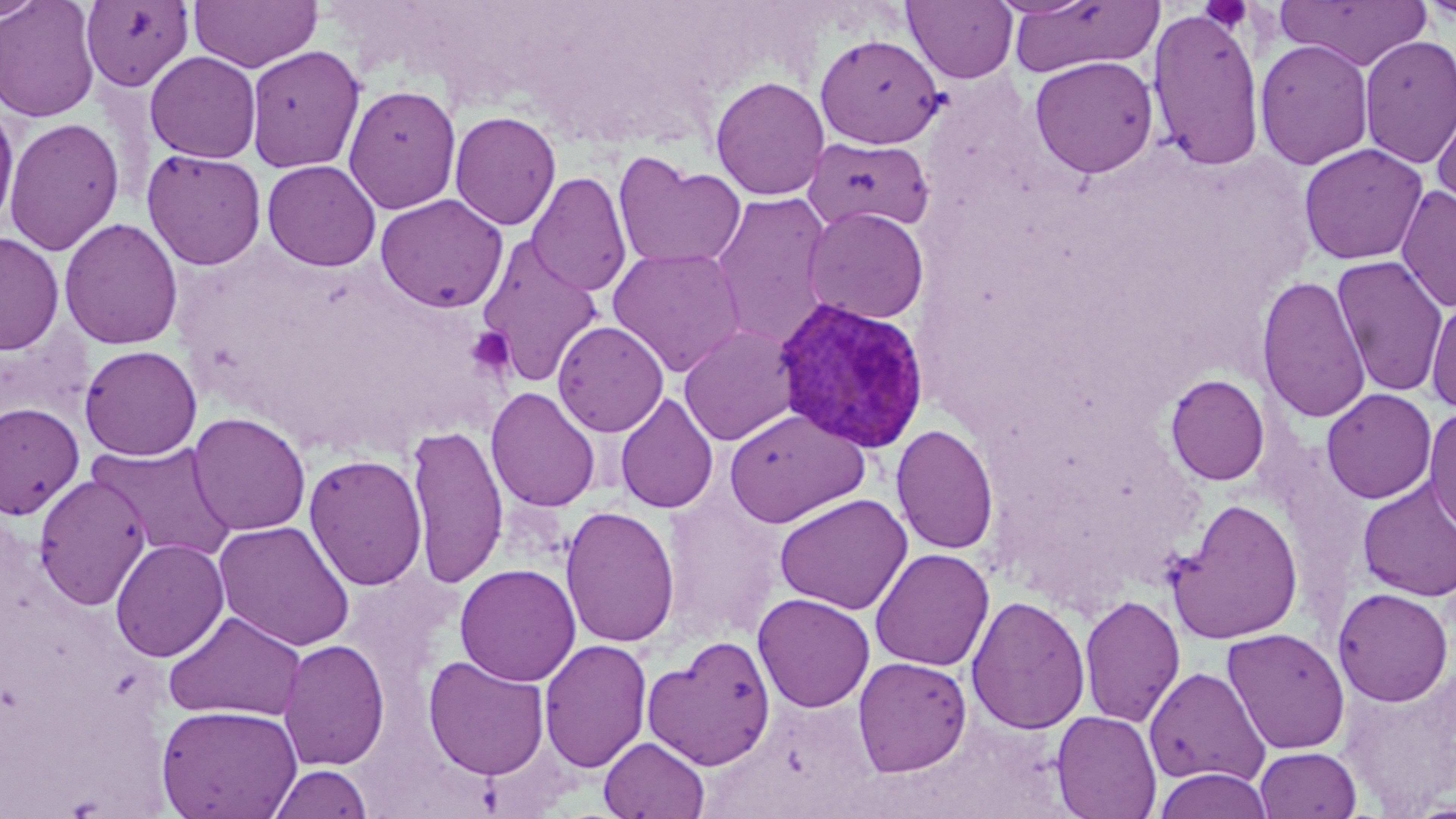
slide_level_diagnosis: Plasmodium vivax
platelet_locations: 'approximate bounding boxes as (x1, y1, x2, y2) in pixels: (1197, 1, 1254, 33), (467, 327, 515, 376)'
modality: light microscopy
stain: May-Grünwald-Giemsa
field_of_view: one of a larger specimen
image_size: 1456×819 pixels
plasmodium_vivax_infected_red_blood_cell_locations: 'approximate bounding boxes as (x1, y1, x2, y2) in pixels: (772, 297, 930, 454)'
preparation: thin blood smear
magnification: 1000x
uninfected_red_blood_cell_locations: 'approximate bounding boxes as (x1, y1, x2, y2) in pixels: (0, 0, 48, 24), (0, 0, 100, 123), (80, 0, 195, 91), (189, 0, 322, 72), (903, 0, 1018, 83), (1006, 0, 1162, 77), (1277, 0, 1431, 70), (1416, 0, 1455, 25), (1147, 8, 1265, 171), (814, 33, 946, 149), (1358, 35, 1456, 168), (1255, 38, 1373, 170), (245, 45, 365, 172), (145, 51, 262, 163), (1029, 55, 1158, 179), (710, 75, 830, 201), (343, 84, 462, 215), (1431, 91, 1456, 215), (0, 100, 20, 233), (448, 111, 562, 230), (3, 116, 124, 255), (802, 136, 934, 233), (1299, 142, 1429, 265), (142, 149, 266, 270), (613, 153, 746, 270), (262, 160, 381, 271), (527, 171, 632, 297), (1396, 184, 1456, 313), (711, 191, 834, 349), (374, 194, 509, 313), (803, 206, 929, 324), (59, 217, 184, 350), (0, 231, 65, 356), (476, 235, 604, 388), (608, 247, 746, 377), (1331, 254, 1449, 397), (1256, 273, 1371, 425), (1425, 294, 1456, 415), (552, 320, 669, 436), (679, 324, 800, 446), (80, 345, 202, 461), (1165, 373, 1270, 486), (486, 386, 601, 512), (1321, 388, 1437, 504), (615, 392, 719, 514), (0, 402, 84, 519), (1423, 404, 1456, 536), (724, 408, 869, 527), (188, 412, 311, 536), (891, 423, 999, 555), (407, 424, 509, 589), (89, 441, 237, 563), (304, 454, 428, 591), (33, 474, 151, 610), (1357, 479, 1456, 601), (774, 493, 912, 615), (1166, 498, 1305, 644), (560, 505, 680, 648), (214, 520, 356, 652), (110, 538, 230, 662), (870, 548, 995, 671), (454, 563, 581, 686), (1333, 587, 1454, 706), (753, 593, 875, 712), (1078, 594, 1186, 728), (966, 595, 1090, 735), (164, 610, 307, 722), (1222, 627, 1350, 755), (643, 635, 777, 771), (278, 638, 390, 770), (539, 638, 652, 773), (422, 655, 551, 780), (853, 656, 973, 777), (1339, 661, 1456, 814), (1144, 665, 1269, 788), (156, 704, 302, 818), (1052, 710, 1162, 819), (599, 736, 710, 819), (1255, 746, 1361, 819), (267, 762, 373, 819), (1153, 768, 1273, 819)'